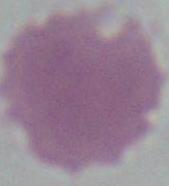
A red blood cell is seen. Captured at 1000x magnification. Photomicrograph.